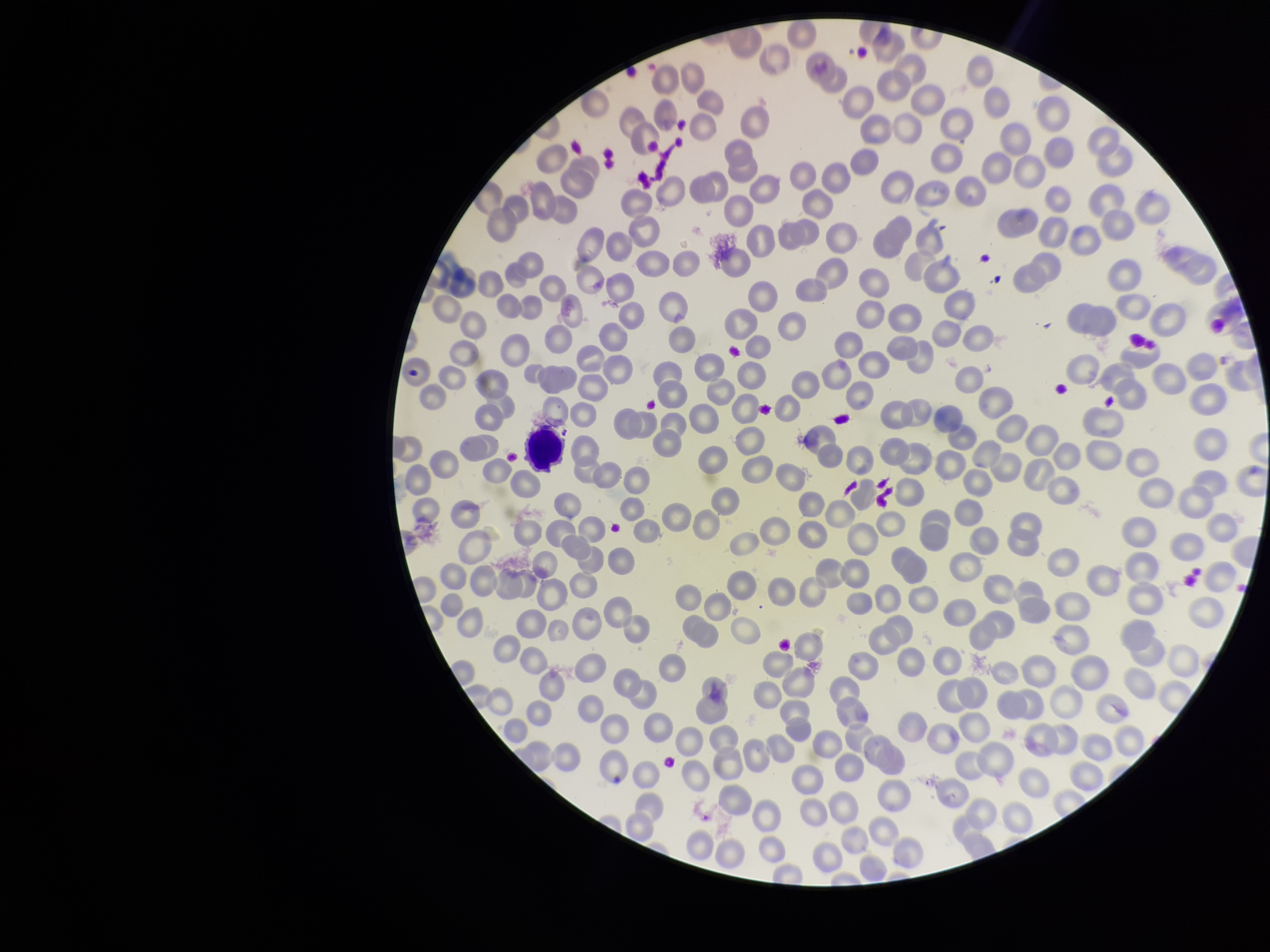

Image is 1270×952 pixels. Preparation: thin smear. Parasitized red blood cells: none seen. Parasitized red blood cell count: 0. One field from this slide. Patient malaria status: positive. Species reported for this patient: Plasmodium falciparum. Red blood cell count: 298. Giemsa stain. Smartphone photograph taken through the eyepiece of a microscope.